Find each WBC.
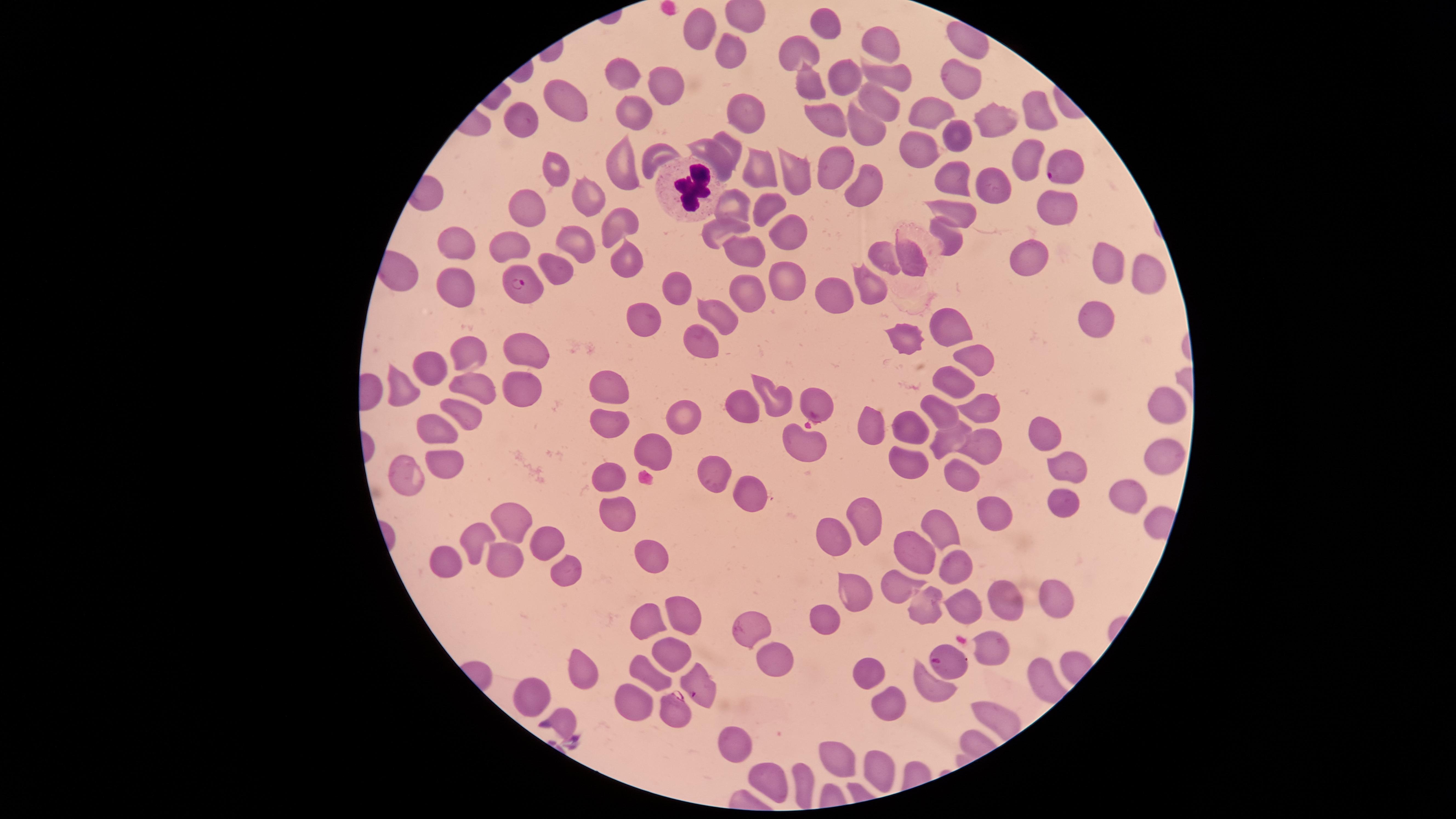

Approximate marker points, in pixels from the top-left corner.
WBCs: (x=694, y=190).

field_of_view: single
presence: malaria parasites seen
visible_region: circular
preparation: thin blood film
species: Plasmodium falciparum
uninfected_RBCs: 'approximate marker points, in pixels from the top-left corner: (x=828, y=21), (x=702, y=30), (x=883, y=40), (x=802, y=48), (x=732, y=49), (x=890, y=74), (x=622, y=76), (x=845, y=76), (x=666, y=78), (x=809, y=81), (x=567, y=101), (x=876, y=103), (x=1035, y=107), (x=634, y=112), (x=933, y=113), (x=746, y=115), (x=824, y=118), (x=526, y=121), (x=995, y=121), (x=860, y=128), (x=952, y=129), (x=731, y=145), (x=919, y=149), (x=653, y=155), (x=1023, y=158), (x=716, y=161), (x=554, y=166), (x=835, y=166), (x=621, y=167), (x=755, y=171), (x=790, y=173), (x=952, y=174), (x=985, y=184), (x=865, y=190), (x=587, y=194), (x=527, y=200), (x=736, y=202), (x=1055, y=205), (x=768, y=206), (x=955, y=214), (x=619, y=220), (x=722, y=228), (x=790, y=233), (x=949, y=234), (x=576, y=236), (x=455, y=240), (x=508, y=241), (x=748, y=255), (x=624, y=258), (x=886, y=259), (x=909, y=259), (x=1104, y=260), (x=1030, y=261), (x=1141, y=267), (x=553, y=273), (x=786, y=284), (x=454, y=289), (x=677, y=289), (x=872, y=289), (x=748, y=293), (x=835, y=295), (x=721, y=314), (x=642, y=321), (x=952, y=321), (x=1099, y=321), (x=911, y=336), (x=702, y=340), (x=471, y=351), (x=978, y=354), (x=528, y=356), (x=432, y=365), (x=601, y=382), (x=956, y=382), (x=479, y=386), (x=401, y=389), (x=527, y=392), (x=776, y=398), (x=743, y=405), (x=982, y=407), (x=941, y=409), (x=1165, y=410), (x=685, y=412), (x=465, y=413), (x=606, y=422), (x=914, y=426), (x=870, y=428), (x=433, y=430), (x=1040, y=435), (x=949, y=436), (x=804, y=443), (x=654, y=446), (x=981, y=450), (x=1157, y=457), (x=907, y=462), (x=441, y=466), (x=1062, y=468), (x=405, y=472), (x=711, y=472), (x=958, y=473), (x=604, y=477), (x=751, y=496), (x=1115, y=496), (x=1056, y=506), (x=612, y=508), (x=995, y=510), (x=869, y=520), (x=510, y=522), (x=944, y=524), (x=476, y=534), (x=544, y=537), (x=834, y=538), (x=911, y=553), (x=647, y=555), (x=500, y=558), (x=441, y=563), (x=561, y=564), (x=955, y=565), (x=902, y=587), (x=851, y=596), (x=1004, y=598), (x=1053, y=598), (x=967, y=604), (x=928, y=607), (x=682, y=609), (x=644, y=615), (x=819, y=620), (x=986, y=646), (x=672, y=653), (x=771, y=660), (x=584, y=667), (x=866, y=669), (x=654, y=672), (x=930, y=687), (x=530, y=693), (x=883, y=698), (x=634, y=702), (x=564, y=717), (x=738, y=748), (x=837, y=755), (x=875, y=766), (x=773, y=778), (x=802, y=783)'
capture: smartphone photograph through the microscope eyepiece
parasitized_RBCs: 'approximate marker points, in pixels from the top-left corner: (x=956, y=74), (x=1064, y=167), (x=518, y=282), (x=749, y=629), (x=946, y=661), (x=696, y=688), (x=673, y=709)'
image_size: 1456×819 pixels
stain: Giemsa